State the preparation type.
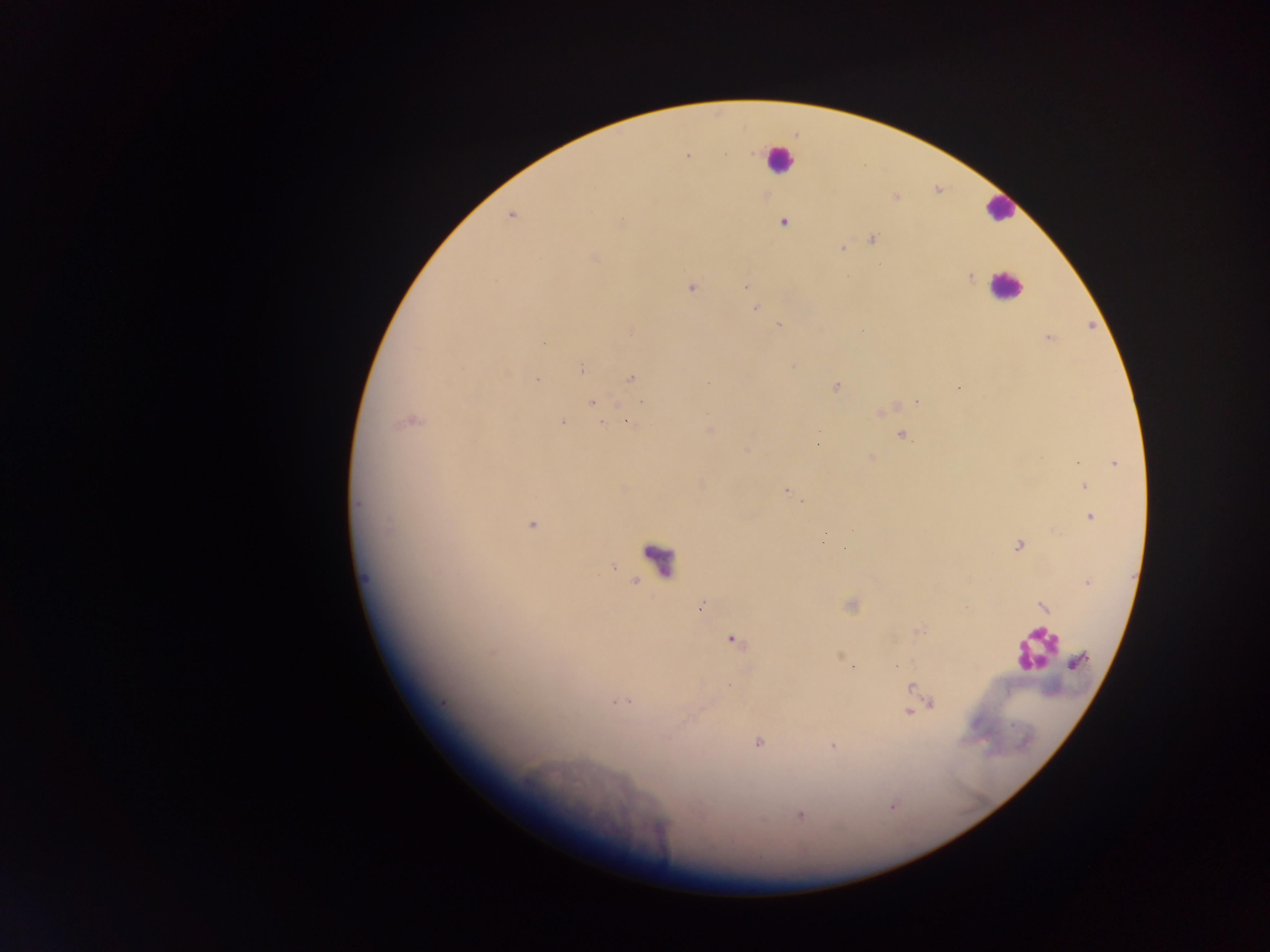
Thick blood film.

Approximate centers as {x, y} in pixels.
Summary:
  - Plasmodium parasite locations: {688, 157}, {511, 215}, {783, 222}, {620, 223}, {873, 240}, {843, 248}, {594, 257}, {970, 277}, {746, 286}, {691, 288}, {751, 300}, {755, 308}, {779, 325}, {1049, 338}, {543, 343}, {793, 366}, {581, 369}, {630, 378}, {538, 379}, {836, 386}, {959, 387}, {641, 402}, {917, 402}, {593, 403}, {410, 422}, {562, 422}, {627, 422}, {602, 423}, {710, 430}, {819, 433}, {901, 436}, {818, 444}, {747, 450}, {1078, 462}, {1116, 463}, {1085, 486}, {786, 491}, {358, 504}, {1091, 517}, {532, 524}, {388, 529}, {1018, 545}, {843, 548}, {1088, 583}, {701, 607}, {1043, 607}, {733, 640}, {493, 652}, {1079, 661}, {729, 686}, {911, 687}, {626, 701}, {615, 702}, {442, 703}, {931, 703}, {907, 712}, {758, 742}, {833, 746}, {799, 815}
  - Leukocyte locations: {778, 159}, {999, 209}, {1005, 285}, {657, 559}, {1035, 650}
  - Image size: 1270×952 pixels
  - Field of view: single
  - Country: Ghana
  - Capture: mobile-phone photograph through a microscope